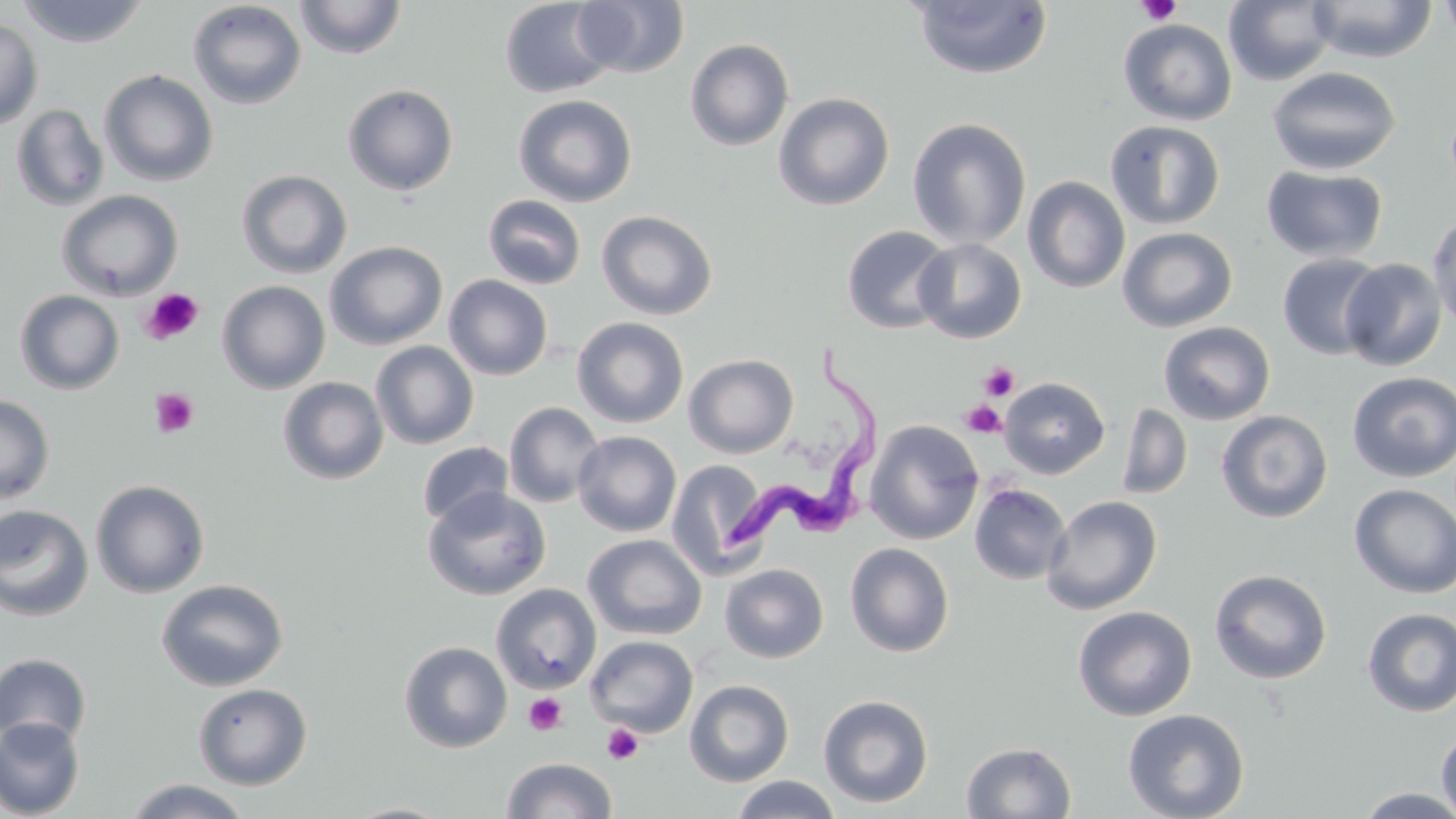

Summary:
  - Coordinate format: approximate bounding boxes as (x1,y1)-(x2,y2) corner pairs in pixels
  - Uninfected red blood cell locations: (294,0)-(407,60), (499,0)-(617,98), (571,0)-(690,78), (1306,0)-(1438,63), (1438,0)-(1456,50), (17,1)-(150,47), (187,1)-(307,109), (909,1)-(1054,79), (1223,1)-(1337,86), (0,18)-(43,130), (1118,18)-(1237,126), (685,39)-(794,151), (1266,66)-(1401,176), (99,69)-(219,187), (342,83)-(459,197), (773,92)-(895,211), (513,94)-(637,207), (11,104)-(109,212), (907,117)-(1031,248), (1105,120)-(1225,230), (1261,164)-(1389,263), (236,169)-(353,279), (1022,176)-(1130,294), (57,189)-(183,301), (483,195)-(587,290), (596,210)-(718,320), (1427,211)-(1456,334), (842,226)-(954,334), (1117,227)-(1237,332), (913,238)-(1026,343), (324,241)-(447,350), (1277,253)-(1388,360), (1340,258)-(1448,371), (443,275)-(553,379), (217,280)-(331,394), (15,290)-(125,395), (572,317)-(689,428), (1158,321)-(1275,425), (370,342)-(479,449), (684,354)-(799,458), (1347,371)-(1456,482), (278,376)-(388,485), (999,377)-(1110,479), (0,395)-(55,505), (504,402)-(605,508), (1116,402)-(1193,500), (1216,409)-(1333,523), (864,420)-(984,545), (573,431)-(681,537), (417,442)-(513,528), (667,459)-(773,579), (90,479)-(210,598), (969,483)-(1071,584), (1349,484)-(1456,598), (424,487)-(551,600), (1041,495)-(1162,615), (0,504)-(94,621), (583,534)-(707,640), (845,542)-(955,657), (720,558)-(955,660), (720,563)-(829,664), (1209,568)-(1333,685), (157,578)-(289,692), (491,583)-(602,693), (1072,606)-(1197,721), (1361,608)-(1456,717), (584,635)-(698,737), (399,640)-(513,753), (1,653)-(92,748), (685,679)-(794,786), (193,682)-(312,789), (818,694)-(934,809), (1122,708)-(1249,819), (0,716)-(85,818), (1436,727)-(1456,819), (961,741)-(1077,818), (501,757)-(618,819), (730,775)-(842,819), (123,777)-(252,818), (1353,787)-(1456,818), (341,802)-(455,819)
  - Platelet locations: (1137,0)-(1182,26), (141,288)-(203,344), (978,361)-(1020,402), (149,388)-(198,439), (961,400)-(1007,439), (523,692)-(568,736), (601,723)-(643,765)
  - Trypanosoma brucei locations: (727,341)-(885,554)
  - Slide-level diagnosis: Trypanosoma brucei
  - Field of view: one of a larger specimen
  - Magnification: 1000x
  - Preparation: thin blood smear
  - Image size: 1456×819 pixels
  - Stain: May-Grünwald-Giemsa
  - Modality: optical microscopy